Classify this cell by malaria status.
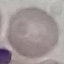

Uninfected.

stain = Giemsa
preparation = thin blood smear
capture = smartphone through the microscope eyepiece
image type = automatically extracted cell patch, resized to 64 × 64 pixels